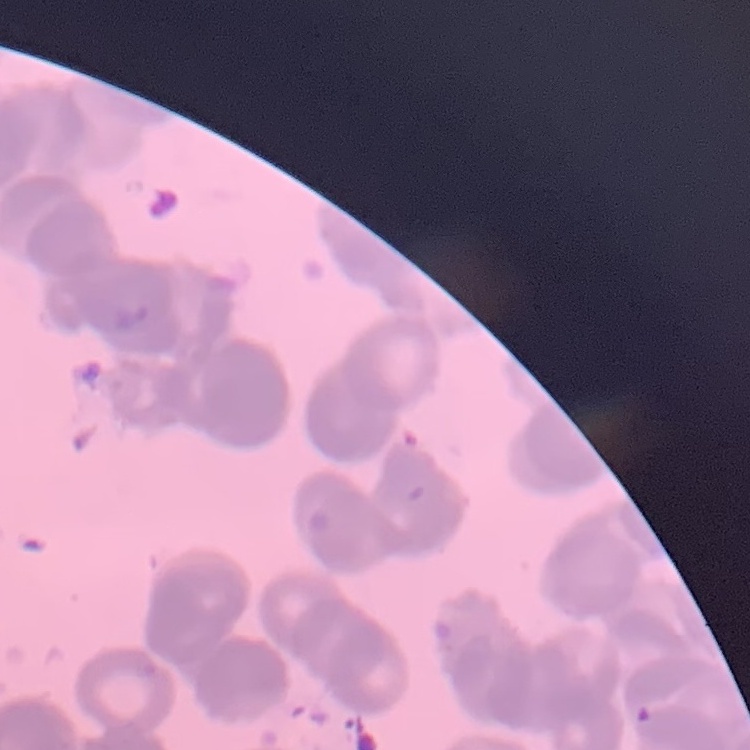

erythrocyte morphology = rouleaux formation
stain = Field's or Giemsa
image type = one tile cut from a larger photomicrograph
preparation = thin blood smear